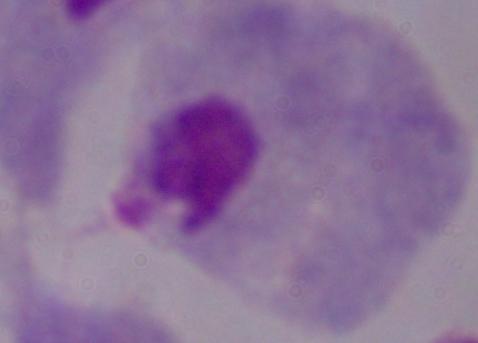

A trichomonad is seen. 1000x magnification. Photomicrograph.